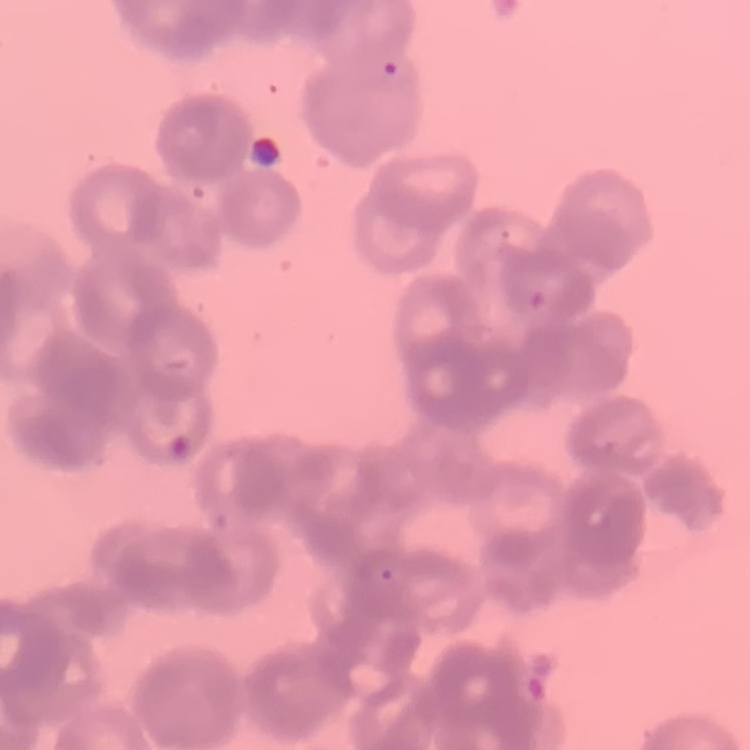

{
  "erythrocyte_morphology": "rouleaux formation",
  "preparation": "thin peripheral smear",
  "stain": "Field's or Giemsa",
  "image_type": "square crop of a larger photomicrograph"
}